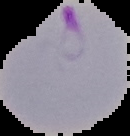
Segmented cell region on a black background. Image is 130×136 pixels. From a thin blood film. Result: Plasmodium parasites identified.